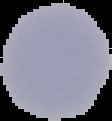
Result: no Plasmodium parasites seen. Image is 112×121 pixels. From a thin blood smear. Cell region segmented out of the field of view; the surrounding area is masked to black.